Give the position of every leukocyte visible.
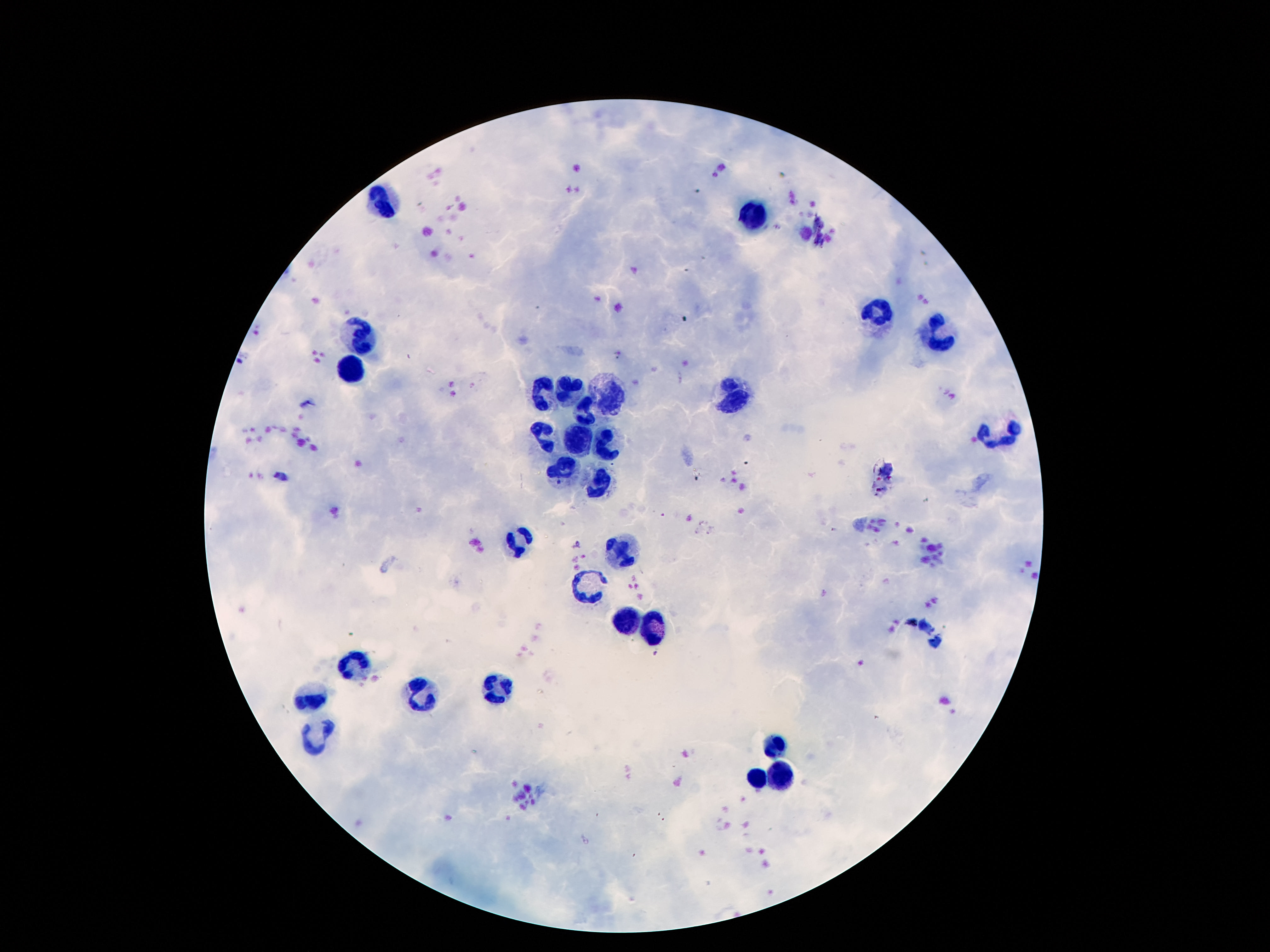

Approximate object centers, in pixels from the top-left corner.
Leukocytes: (x=382, y=200), (x=753, y=217), (x=877, y=317), (x=937, y=334), (x=363, y=341), (x=352, y=375), (x=569, y=390), (x=543, y=392), (x=611, y=396), (x=734, y=399), (x=585, y=414), (x=1000, y=434), (x=543, y=438), (x=604, y=440), (x=578, y=442), (x=564, y=467), (x=597, y=488), (x=520, y=541), (x=622, y=553), (x=590, y=587), (x=627, y=622), (x=653, y=630), (x=352, y=664), (x=496, y=688), (x=422, y=695), (x=312, y=697), (x=314, y=732), (x=779, y=745), (x=783, y=774), (x=758, y=778).

{
  "preparation": "thick blood smear",
  "magnification": "100x",
  "capture": "smartphone camera through the microscope eyepiece",
  "field_of_view": "single",
  "image_size": "1270×952 pixels",
  "patient_malaria_status": "negative",
  "stain": "Giemsa"
}